State which parasite is depicted.
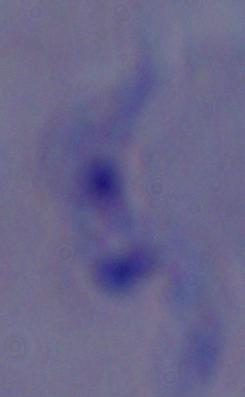
This is a trypanosome.

1000x magnification. Photomicrograph.